Name the cell type shown.
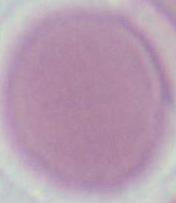

An erythrocyte.

Summary:
  - Modality: micrograph
  - Magnification: 1000x